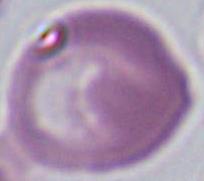

magnification: 1000x
modality: micrograph
identification: red blood cell